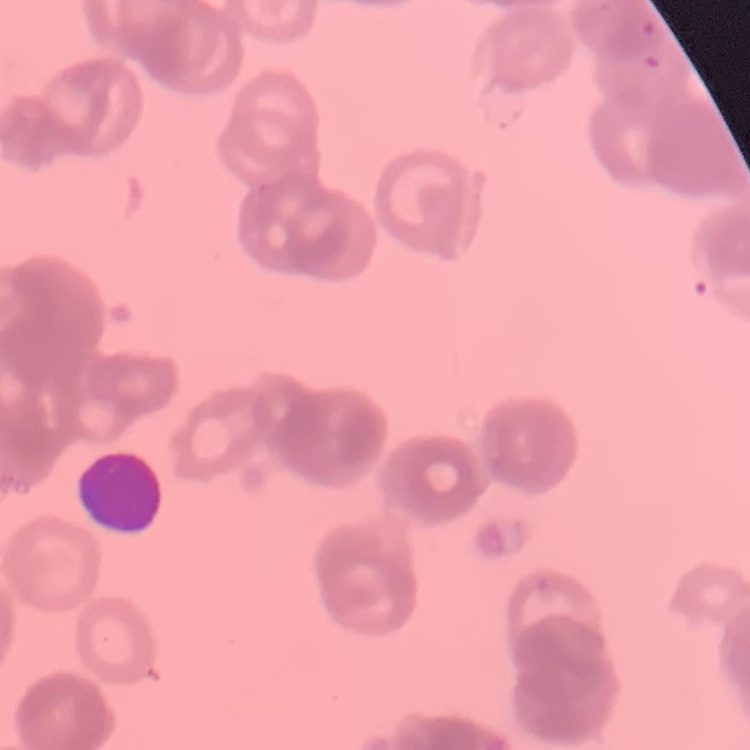
red blood cell morphology = rouleaux formation
preparation = thin blood film
stain = Field's or Giemsa
image type = square crop of a larger photomicrograph